Assess the morphology of the erythrocytes.
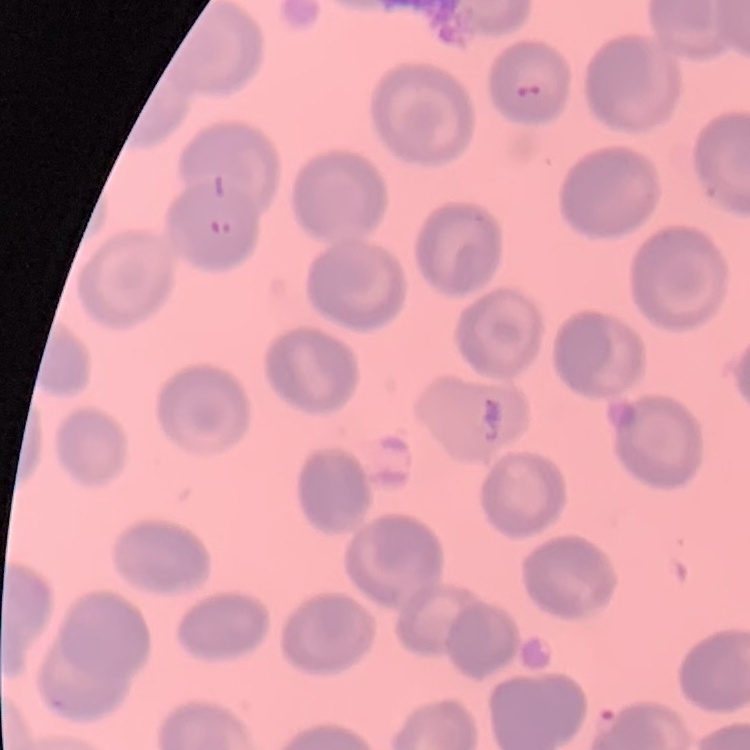
No rouleaux formation.

One tile cut from a larger photomicrograph. Stained with either Field's or Giemsa. Thin peripheral smear.